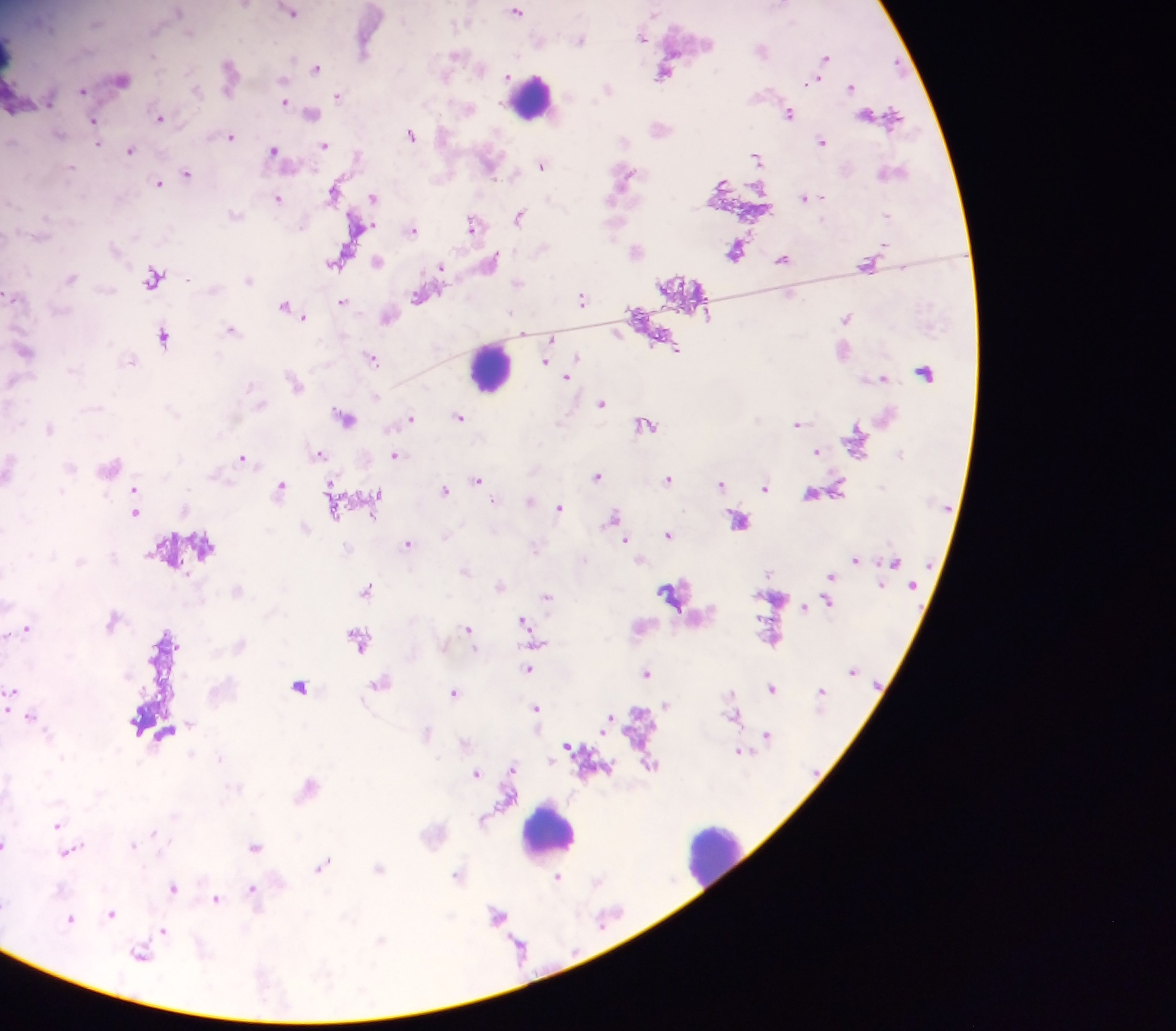

Approximate centers as {x, y} in pixels. Leukocyte locations: {12, 57}, {532, 95}, {491, 366}, {549, 828}, {713, 855}. Malaria parasite locations: {516, 10}, {292, 11}, {642, 36}, {581, 39}, {365, 42}, {762, 48}, {457, 54}, {826, 55}, {317, 66}, {666, 70}, {229, 72}, {122, 78}, {817, 79}, {852, 85}, {609, 88}, {84, 90}, {338, 95}, {285, 101}, {791, 111}, {311, 112}, {886, 114}, {161, 117}, {95, 121}, {661, 127}, {411, 133}, {231, 135}, {823, 139}, {325, 144}, {130, 149}, {275, 150}, {358, 154}, {757, 156}, {490, 163}, {542, 163}, {188, 173}, {624, 175}, {160, 182}, {335, 189}, {373, 196}, {807, 196}, {278, 197}, {520, 214}, {359, 224}, {474, 224}, {413, 228}, {637, 248}, {736, 249}, {784, 257}, {494, 258}, {378, 260}, {336, 261}, {869, 263}, {441, 266}, {154, 276}, {421, 295}, {583, 298}, {343, 300}, {287, 306}, {305, 314}, {388, 316}, {847, 317}, {233, 329}, {524, 333}, {165, 335}, {553, 338}, {25, 350}, {373, 357}, {546, 359}, {568, 375}, {882, 377}, {296, 382}, {602, 401}, {345, 415}, {411, 416}, {460, 416}, {797, 422}, {646, 423}, {50, 426}, {817, 450}, {320, 452}, {396, 454}, {243, 456}, {598, 474}, {479, 478}, {669, 478}, {332, 483}, {722, 483}, {282, 484}, {766, 487}, {446, 488}, {136, 490}, {813, 492}, {378, 494}, {531, 499}, {560, 506}, {334, 509}, {136, 511}, {614, 515}, {740, 518}, {669, 532}, {627, 539}, {409, 542}, {856, 558}, {466, 569}, {832, 575}, {500, 584}, {368, 587}, {674, 593}, {548, 596}, {828, 599}, {804, 605}, {525, 620}, {28, 628}, {469, 628}, {7, 634}, {359, 637}, {529, 668}, {648, 672}, {380, 682}, {300, 685}, {773, 687}, {12, 689}, {822, 689}, {454, 691}, {667, 704}, {537, 707}, {10, 708}, {32, 715}, {736, 715}, {610, 718}, {768, 733}, {570, 746}, {741, 750}, {650, 763}, {512, 768}, {476, 772}, {57, 824}, {6, 842}, {255, 846}, {69, 851}, {324, 863}, {379, 867}, {459, 874}, {558, 876}, {173, 886}, {254, 888}, {217, 898}, {112, 912}, {497, 913}, {71, 918}, {164, 930}, {141, 953}. Single field of view. Mobile-phone photograph taken through the microscope. Collected in Ghana. Image is 1176×1031 pixels. Thick blood film.